Identify the parasite.
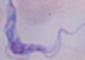
A trypanosome.

modality = micrograph
magnification = 1000x